Report the malaria status of this cell.
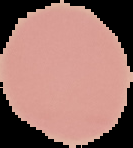
Uninfected.

image_size: 133×148 pixels
image_type: segmented cell region on a black background
preparation: thin blood smear